Comment on the morphology of the erythrocytes.
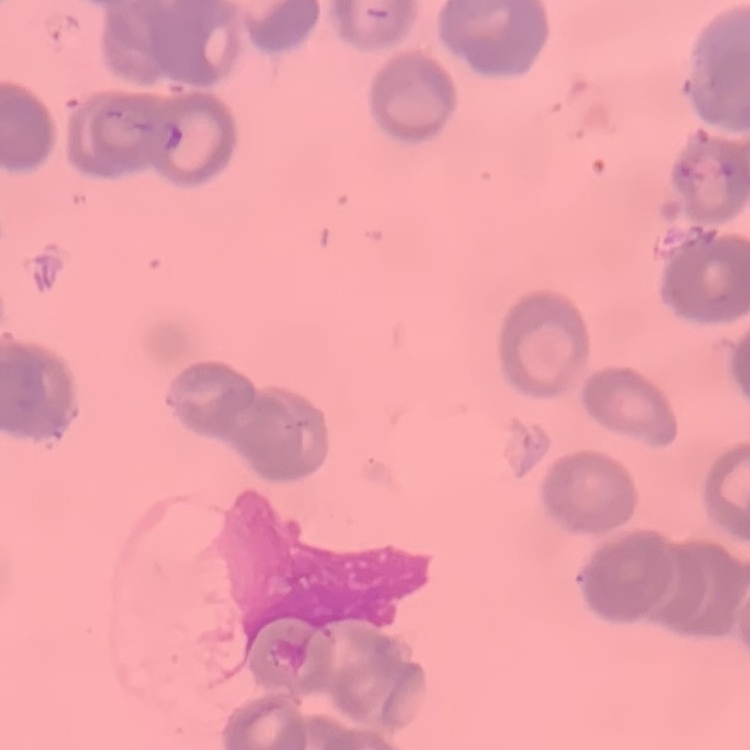
They show rouleaux formation.

Thin peripheral smear. One tile cut from a larger photomicrograph. Field's or Giemsa stain.